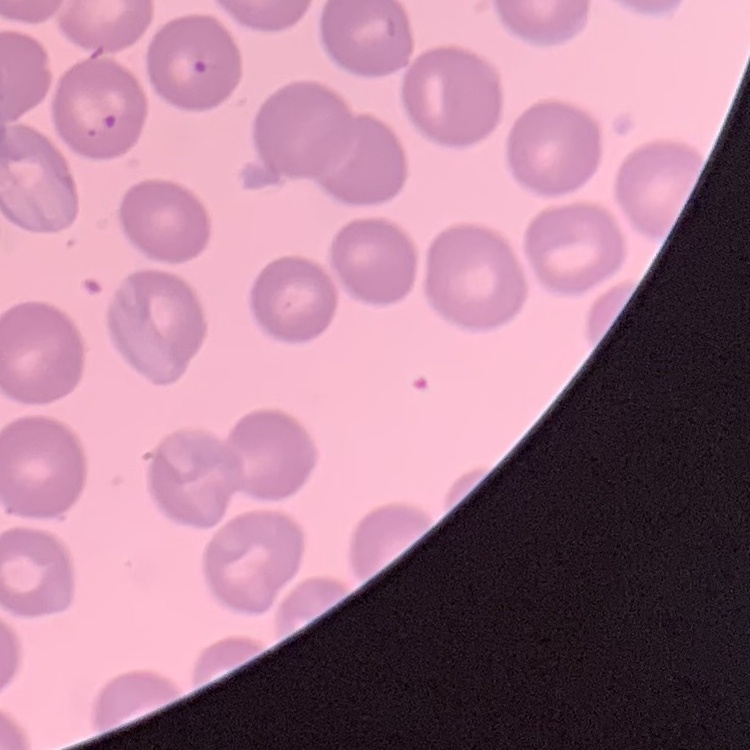

Summary:
  - Erythrocyte morphology: no rouleaux formation
  - Preparation: thin peripheral smear
  - Stain: Field's or Giemsa
  - Image type: one tile cut from a larger photomicrograph